State the blood parasite species.
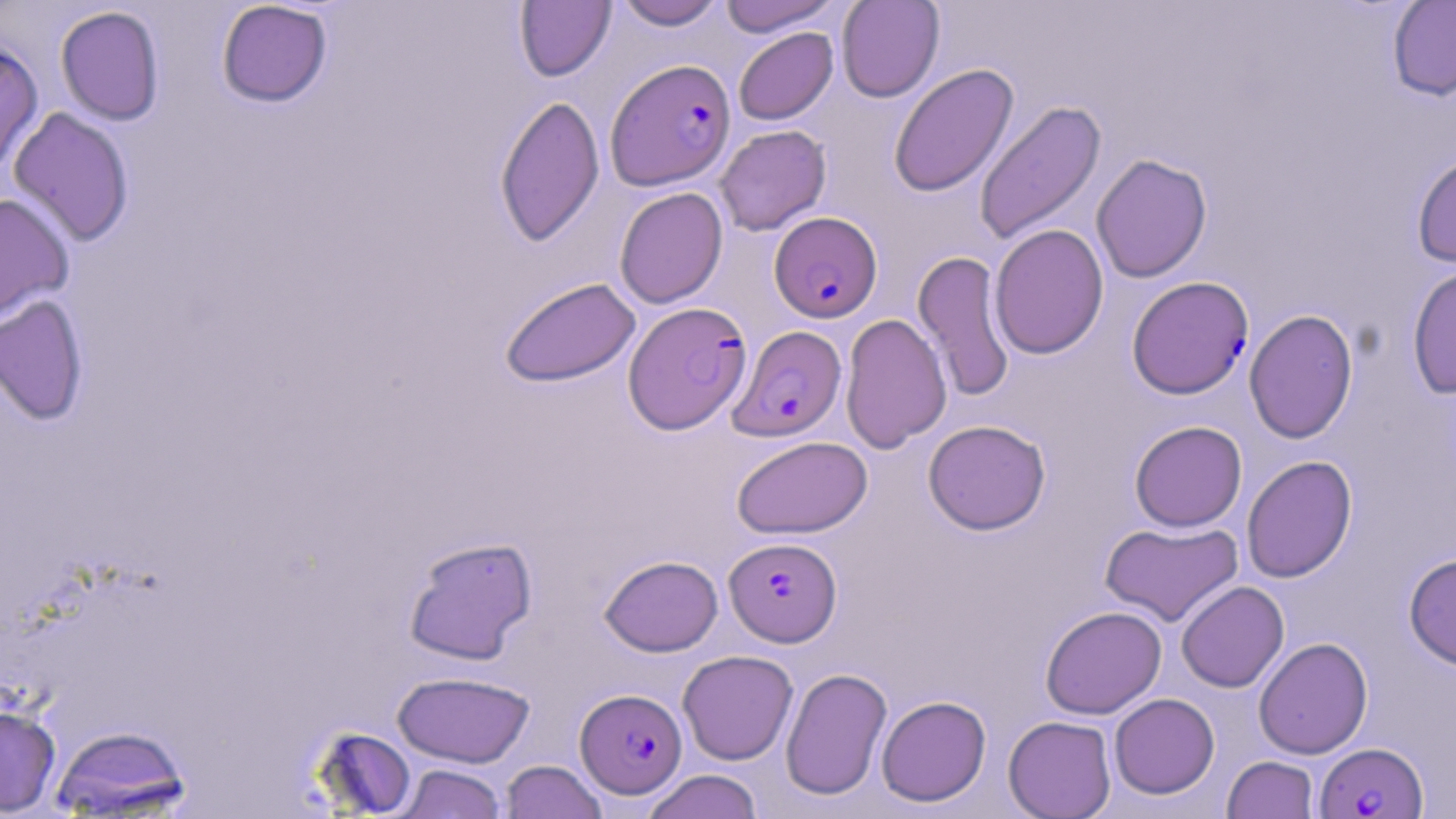

Plasmodium falciparum.

Summary:
  - Coordinate format: approximate bounding boxes as (x1, y1, x2, y2) in pixels
  - Plasmodium falciparum-infected red blood cell locations: (605, 58, 736, 190), (769, 211, 882, 323), (1127, 276, 1254, 399), (623, 301, 751, 434), (729, 325, 847, 442), (724, 537, 842, 647), (575, 688, 687, 798), (1314, 742, 1428, 818)
  - Uninfected red blood cell locations: (615, 0, 727, 30), (719, 0, 841, 37), (836, 0, 945, 103), (1387, 0, 1456, 101), (216, 1, 333, 108), (515, 1, 615, 81), (55, 5, 165, 126), (733, 27, 838, 125), (0, 41, 43, 174), (889, 63, 1019, 198), (494, 94, 605, 247), (974, 100, 1107, 246), (8, 107, 135, 247), (714, 124, 831, 236), (1411, 151, 1456, 268), (1091, 153, 1213, 283), (614, 187, 728, 309), (0, 193, 74, 323), (989, 224, 1109, 359), (912, 250, 1016, 402), (1407, 262, 1456, 399), (499, 276, 641, 388), (0, 294, 89, 426), (1244, 308, 1358, 444), (840, 313, 952, 453), (923, 419, 1051, 535), (1129, 420, 1247, 532), (731, 435, 872, 539), (1241, 455, 1358, 583), (1100, 521, 1243, 627), (403, 535, 538, 665), (1404, 552, 1456, 671), (600, 555, 723, 656), (1176, 581, 1289, 693), (1040, 606, 1167, 719), (1253, 637, 1373, 759), (678, 650, 798, 765), (780, 667, 892, 801), (393, 671, 535, 767), (1108, 693, 1219, 799), (876, 695, 991, 807), (0, 704, 61, 816), (1003, 715, 1117, 818), (49, 725, 192, 816), (311, 727, 417, 817), (1222, 756, 1319, 818), (500, 761, 607, 818), (395, 764, 507, 818), (641, 769, 764, 819)
  - Stain: May-Grünwald-Giemsa
  - Modality: light microscopy
  - Preparation: thin blood smear
  - Image size: 1456×819 pixels
  - Field of view: single
  - Magnification: 1000x